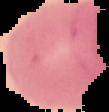 Image is 109×112 pixels. Result: negative for Plasmodium parasites. From a thin blood smear. Cell region segmented out of the field of view; the surrounding area is masked to black.